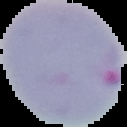 Result: Plasmodium parasites detected. Image is 127×127 pixels. From a thin blood smear. Segmented cell region on a black background.